Identify the preparation type.
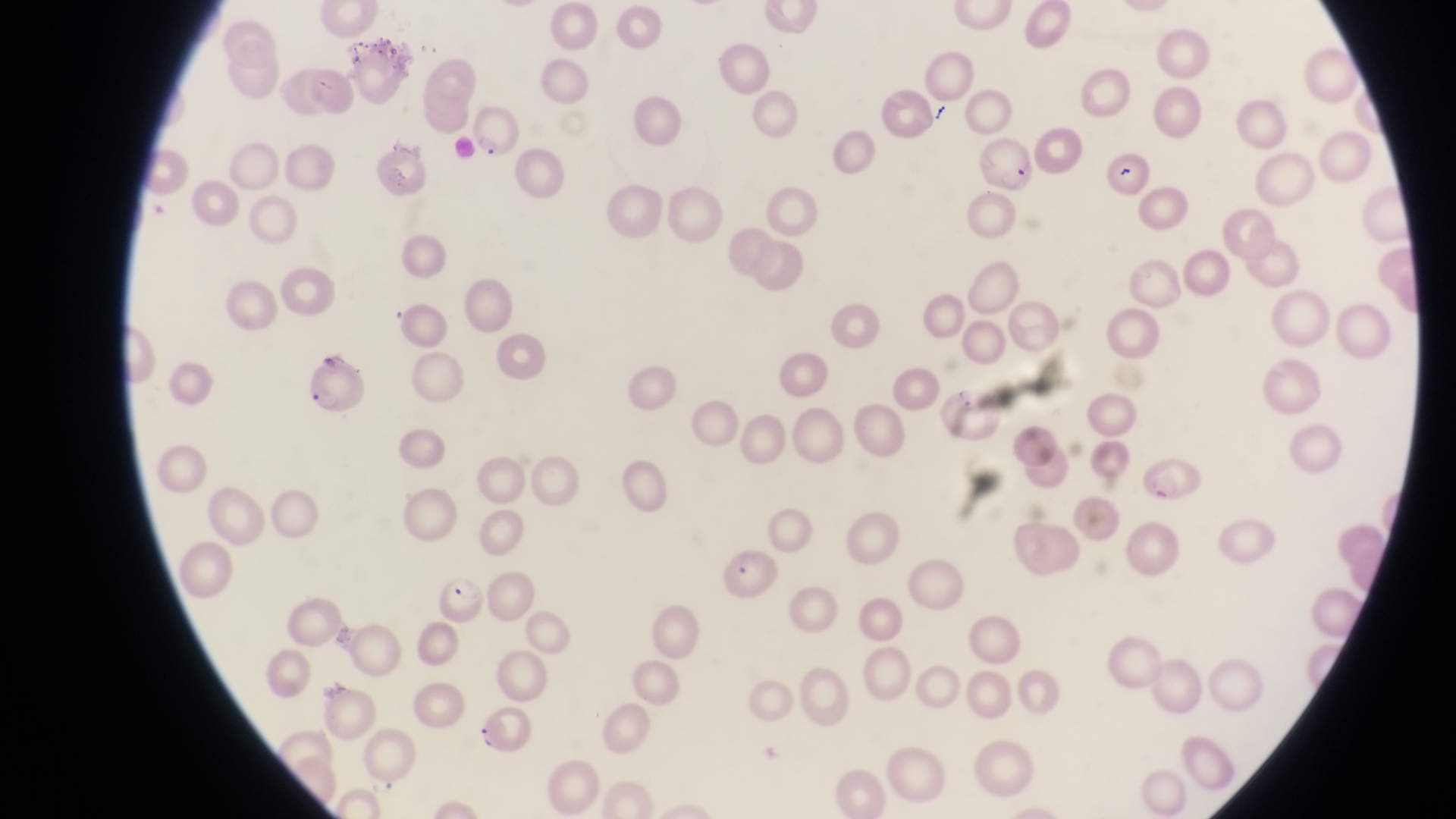
This is a thin smear.

parasitised red blood cell locations = approximate bounding boxes as [left, top, right, bottom] in pixels: [465, 106, 521, 162], [975, 135, 1036, 195], [1138, 457, 1210, 507], [719, 551, 779, 600], [438, 573, 485, 626], [479, 703, 542, 761]
country = Uganda
field of view = single
image size = 1456×819 pixels
capture = smartphone photograph through the eyepiece of an Olympus CX-23 microscope
artifact (platelet-like body, stain precipitate, or debris) locations = approximate bounding boxes as [left, top, right, bottom] in pixels: [1115, 159, 1138, 183]
magnification = 1000x